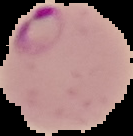
Malaria status: parasitized. Segmented cell region on a black background. From a thin blood smear. Image is 133×136 pixels.